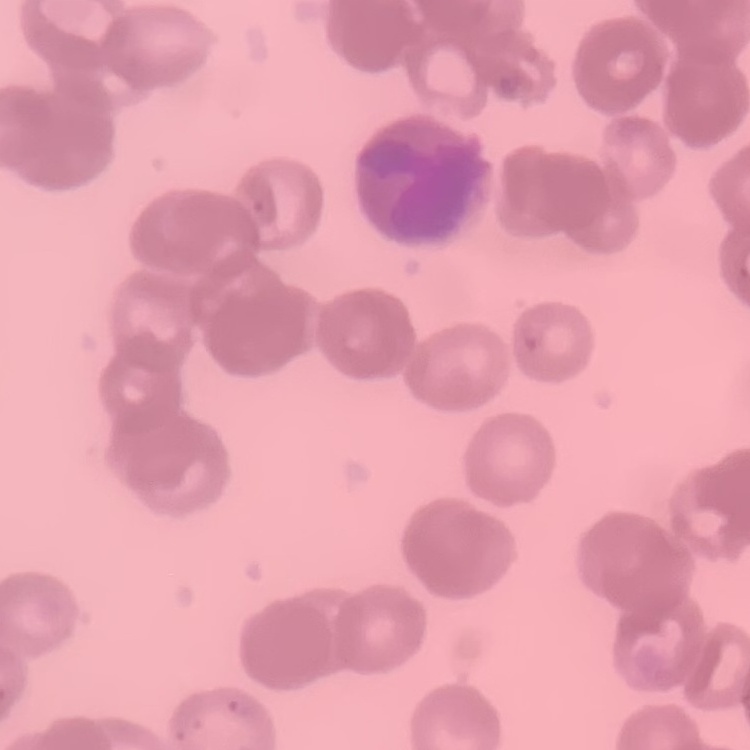
Summary:
  - Red blood cell morphology: rouleaux formation
  - Image type: square crop of a larger photomicrograph
  - Stain: Field's or Giemsa
  - Preparation: thin peripheral smear